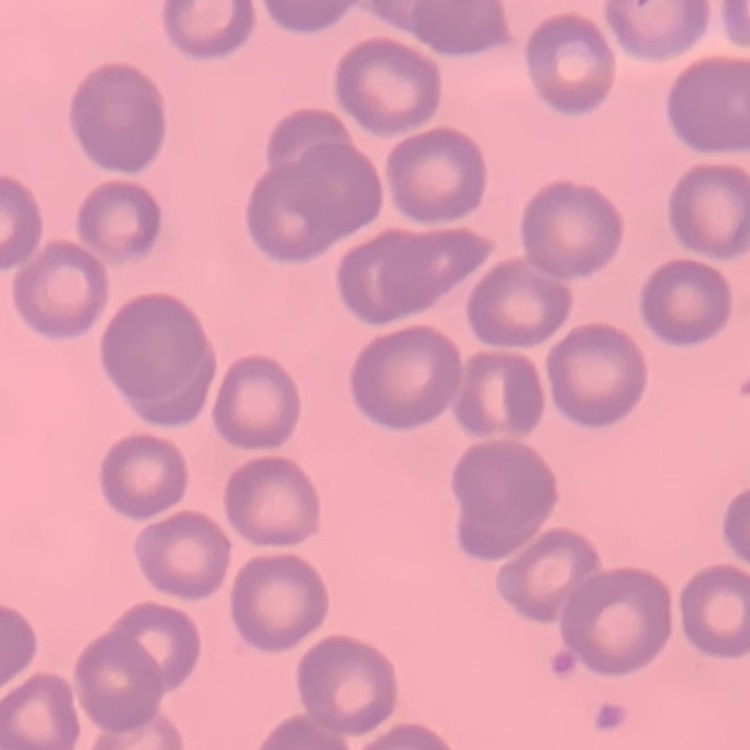
erythrocyte morphology = no rouleaux formation
image type = one tile cut from a larger photomicrograph
stain = Field's or Giemsa
preparation = thin peripheral smear